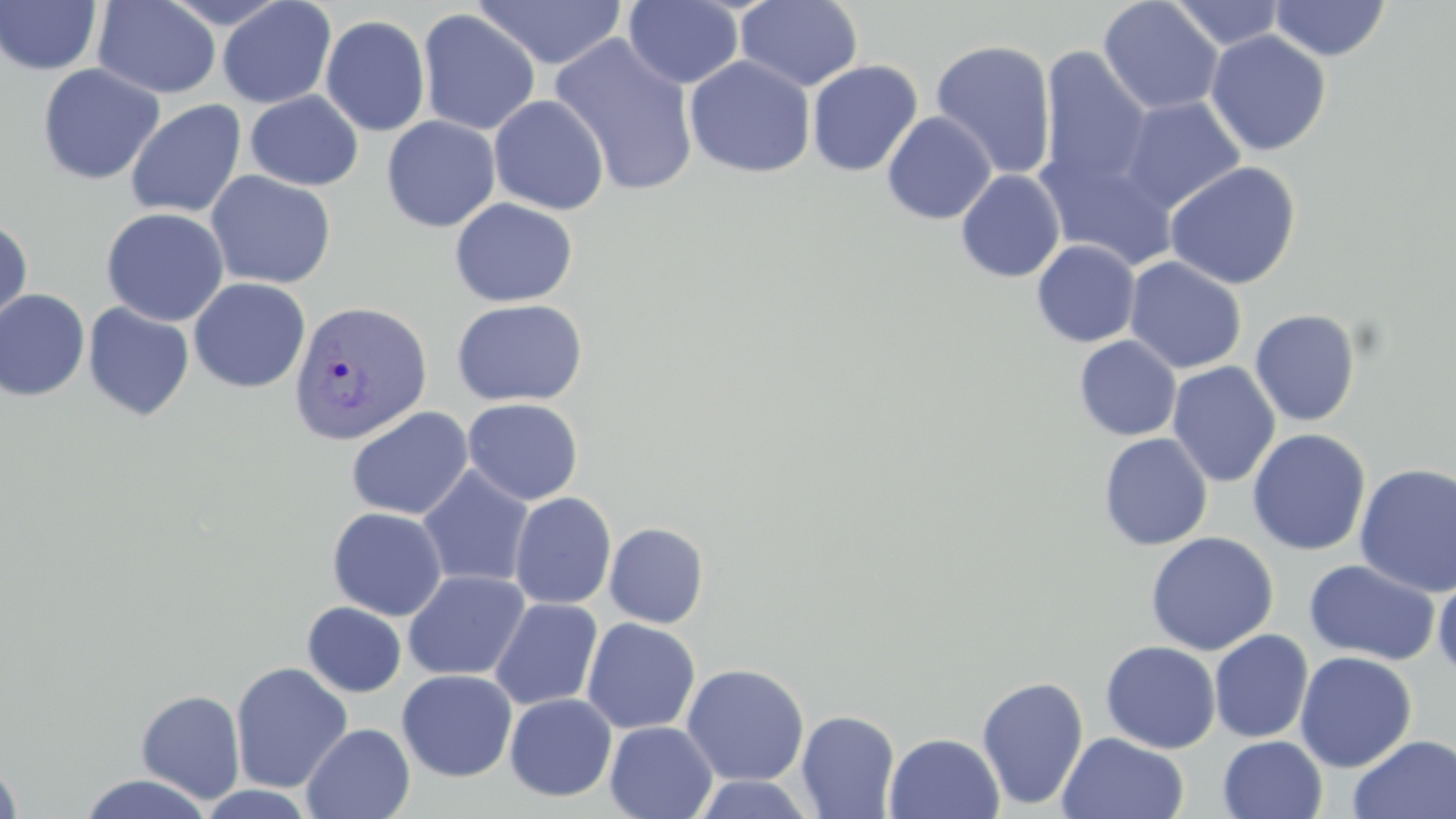
slide-level diagnosis = Plasmodium vivax
uninfected red blood cell locations = approximate bounding boxes as named x1/y1/x2/y2 corners in pixels: (x1=217, y1=0, x2=337, y2=109), (x1=623, y1=0, x2=745, y2=89), (x1=734, y1=0, x2=864, y2=93), (x1=1168, y1=0, x2=1287, y2=51), (x1=0, y1=1, x2=102, y2=75), (x1=92, y1=1, x2=222, y2=99), (x1=473, y1=1, x2=627, y2=70), (x1=1098, y1=1, x2=1224, y2=116), (x1=1269, y1=1, x2=1390, y2=61), (x1=417, y1=10, x2=541, y2=136), (x1=320, y1=15, x2=431, y2=136), (x1=1206, y1=30, x2=1331, y2=156), (x1=550, y1=33, x2=699, y2=197), (x1=930, y1=39, x2=1057, y2=179), (x1=1038, y1=45, x2=1153, y2=193), (x1=684, y1=56, x2=815, y2=178), (x1=806, y1=60, x2=923, y2=177), (x1=37, y1=63, x2=165, y2=185), (x1=245, y1=90, x2=363, y2=191), (x1=488, y1=94, x2=610, y2=215), (x1=1118, y1=96, x2=1247, y2=215), (x1=125, y1=99, x2=246, y2=218), (x1=882, y1=111, x2=997, y2=225), (x1=382, y1=115, x2=501, y2=232), (x1=1036, y1=150, x2=1179, y2=271), (x1=1164, y1=161, x2=1302, y2=290), (x1=956, y1=169, x2=1065, y2=283), (x1=205, y1=170, x2=336, y2=289), (x1=450, y1=198, x2=578, y2=307), (x1=101, y1=207, x2=229, y2=326), (x1=0, y1=218, x2=33, y2=329), (x1=1032, y1=240, x2=1140, y2=347), (x1=1124, y1=256, x2=1247, y2=374), (x1=188, y1=277, x2=311, y2=393), (x1=0, y1=289, x2=91, y2=401), (x1=451, y1=298, x2=587, y2=407), (x1=83, y1=302, x2=195, y2=422), (x1=1249, y1=309, x2=1362, y2=427), (x1=1074, y1=335, x2=1181, y2=441), (x1=1167, y1=361, x2=1281, y2=488), (x1=462, y1=397, x2=583, y2=505), (x1=346, y1=406, x2=473, y2=520), (x1=1247, y1=428, x2=1371, y2=556), (x1=1098, y1=432, x2=1213, y2=551), (x1=1354, y1=463, x2=1456, y2=598), (x1=417, y1=465, x2=535, y2=589), (x1=509, y1=491, x2=617, y2=609), (x1=327, y1=507, x2=448, y2=620), (x1=604, y1=522, x2=709, y2=628), (x1=1145, y1=531, x2=1279, y2=655), (x1=1303, y1=559, x2=1441, y2=666), (x1=403, y1=569, x2=530, y2=681), (x1=1432, y1=569, x2=1456, y2=682), (x1=489, y1=598, x2=603, y2=711), (x1=302, y1=602, x2=406, y2=697), (x1=581, y1=618, x2=701, y2=734), (x1=1209, y1=629, x2=1314, y2=743), (x1=1100, y1=640, x2=1221, y2=754), (x1=1294, y1=651, x2=1417, y2=772), (x1=230, y1=661, x2=353, y2=793), (x1=681, y1=663, x2=809, y2=786), (x1=397, y1=669, x2=518, y2=782), (x1=976, y1=675, x2=1089, y2=811), (x1=136, y1=689, x2=245, y2=803), (x1=504, y1=694, x2=617, y2=801), (x1=796, y1=709, x2=900, y2=819), (x1=604, y1=721, x2=718, y2=819), (x1=301, y1=723, x2=415, y2=819), (x1=884, y1=732, x2=1005, y2=819), (x1=1057, y1=732, x2=1190, y2=819), (x1=1347, y1=734, x2=1456, y2=818), (x1=1217, y1=735, x2=1328, y2=819), (x1=0, y1=757, x2=24, y2=819), (x1=77, y1=773, x2=215, y2=819), (x1=692, y1=774, x2=818, y2=818), (x1=197, y1=785, x2=316, y2=818)
Plasmodium vivax-infected red blood cell locations = approximate bounding boxes as named x1/y1/x2/y2 corners in pixels: (x1=289, y1=299, x2=433, y2=447)
preparation = thin blood smear
field of view = one of a larger specimen
image size = 1456×819 pixels
magnification = 1000x
modality = light microscopy
stain = May-Grünwald-Giemsa